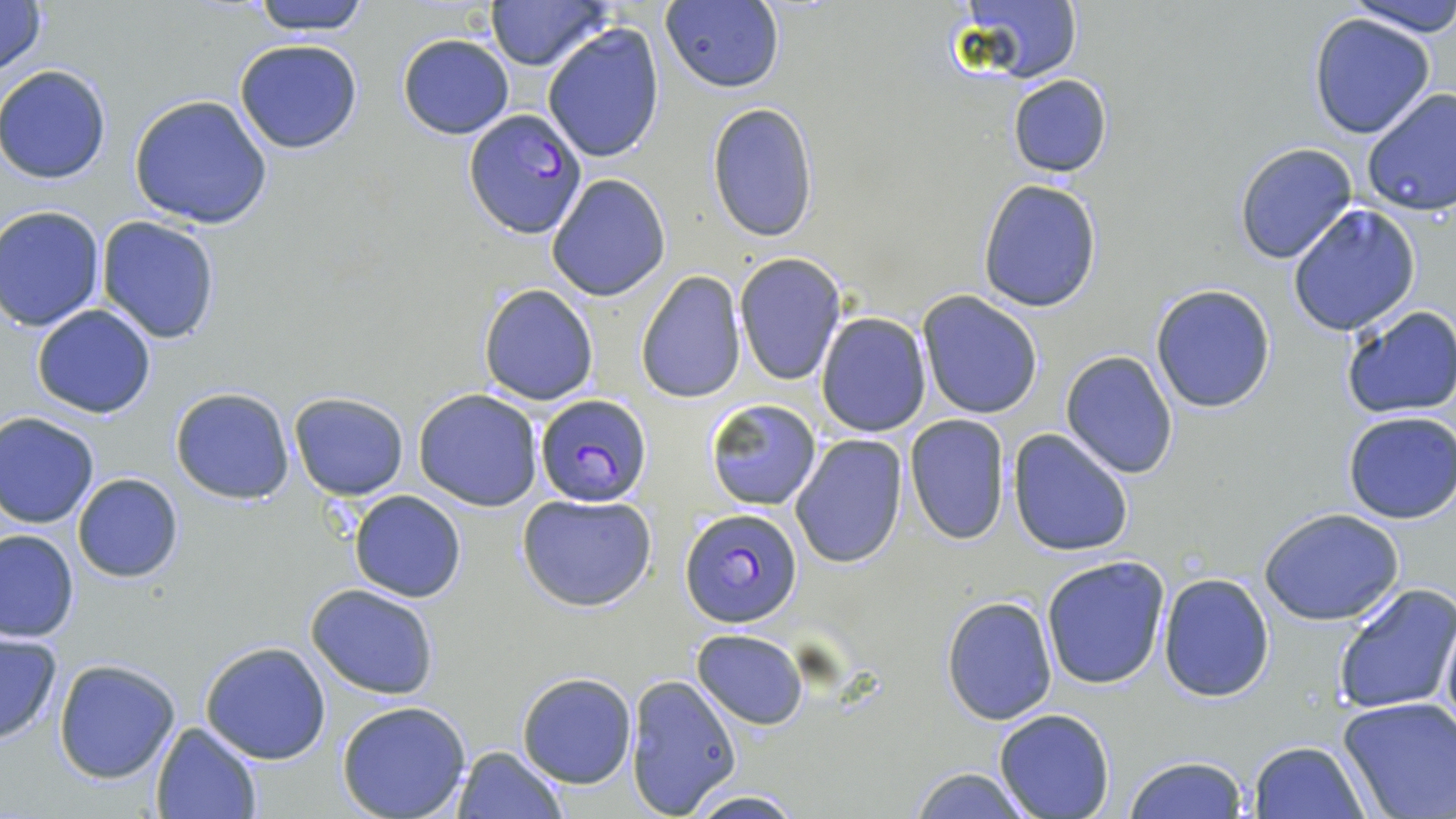

{
  "plasmodium_falciparum_infected_red_blood_cell_locations": "approximate bounding boxes as (x1,y1)-(x2,y2) corner pairs in pixels: (463,110)-(588,240), (533,393)-(652,507), (681,509)-(803,629)",
  "slide_level_diagnosis": "Plasmodium falciparum",
  "uninfected_red_blood_cell_locations": "approximate bounding boxes as (x1,y1)-(x2,y2) corner pairs in pixels: (0,0)-(48,82), (250,0)-(372,35), (661,0)-(786,94), (1340,0)-(1456,36), (484,1)-(612,71), (962,1)-(1082,84), (1309,14)-(1436,139), (542,23)-(666,163), (398,34)-(514,138), (233,38)-(364,153), (0,64)-(112,183), (1007,73)-(1115,180), (1359,88)-(1456,217), (129,93)-(273,230), (705,102)-(820,243), (1234,142)-(1359,264), (546,174)-(671,302), (977,180)-(1104,313), (1286,204)-(1422,338), (0,205)-(105,330), (96,216)-(222,344), (734,252)-(848,388), (635,270)-(747,404), (478,282)-(600,406), (1150,284)-(1277,414), (916,292)-(1043,420), (31,304)-(158,418), (1341,306)-(1456,420), (814,313)-(931,436), (1061,350)-(1179,479), (170,386)-(294,504), (413,388)-(545,512), (288,392)-(409,499), (704,398)-(823,511), (1,410)-(101,528), (1343,410)-(1456,524), (904,414)-(1010,544), (1007,427)-(1136,557), (789,434)-(907,568), (72,473)-(185,583), (350,490)-(467,603), (517,492)-(658,613), (1260,508)-(1406,625), (0,528)-(78,643), (1040,555)-(1170,689), (1158,571)-(1274,703), (305,583)-(441,699), (1333,583)-(1456,718), (942,596)-(1058,725), (1439,610)-(1456,741), (692,628)-(808,729), (0,630)-(63,744), (199,640)-(332,765), (53,659)-(181,784), (516,672)-(636,789), (625,674)-(743,816), (1337,696)-(1456,819), (337,699)-(472,819), (993,709)-(1114,819), (150,721)-(262,819), (1246,741)-(1370,819), (452,746)-(566,818), (1123,754)-(1250,819), (907,765)-(1031,819), (682,789)-(809,819)",
  "image_size": "1456×819 pixels",
  "preparation": "thin blood smear",
  "modality": "optical microscopy",
  "field_of_view": "one of a larger specimen",
  "stain": "May-Grünwald-Giemsa",
  "magnification": "1000x"
}